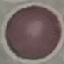

malaria status = uninfected
stain = Giemsa
image type = automatically extracted cell patch, resized to 64 × 64 pixels
preparation = thin blood smear
capture = smartphone through the microscope eyepiece